Identify the parasite.
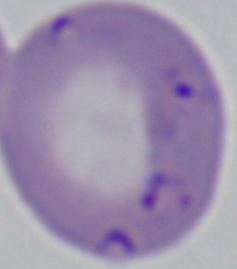
This is Babesia.

magnification = 1000x
modality = photomicrograph